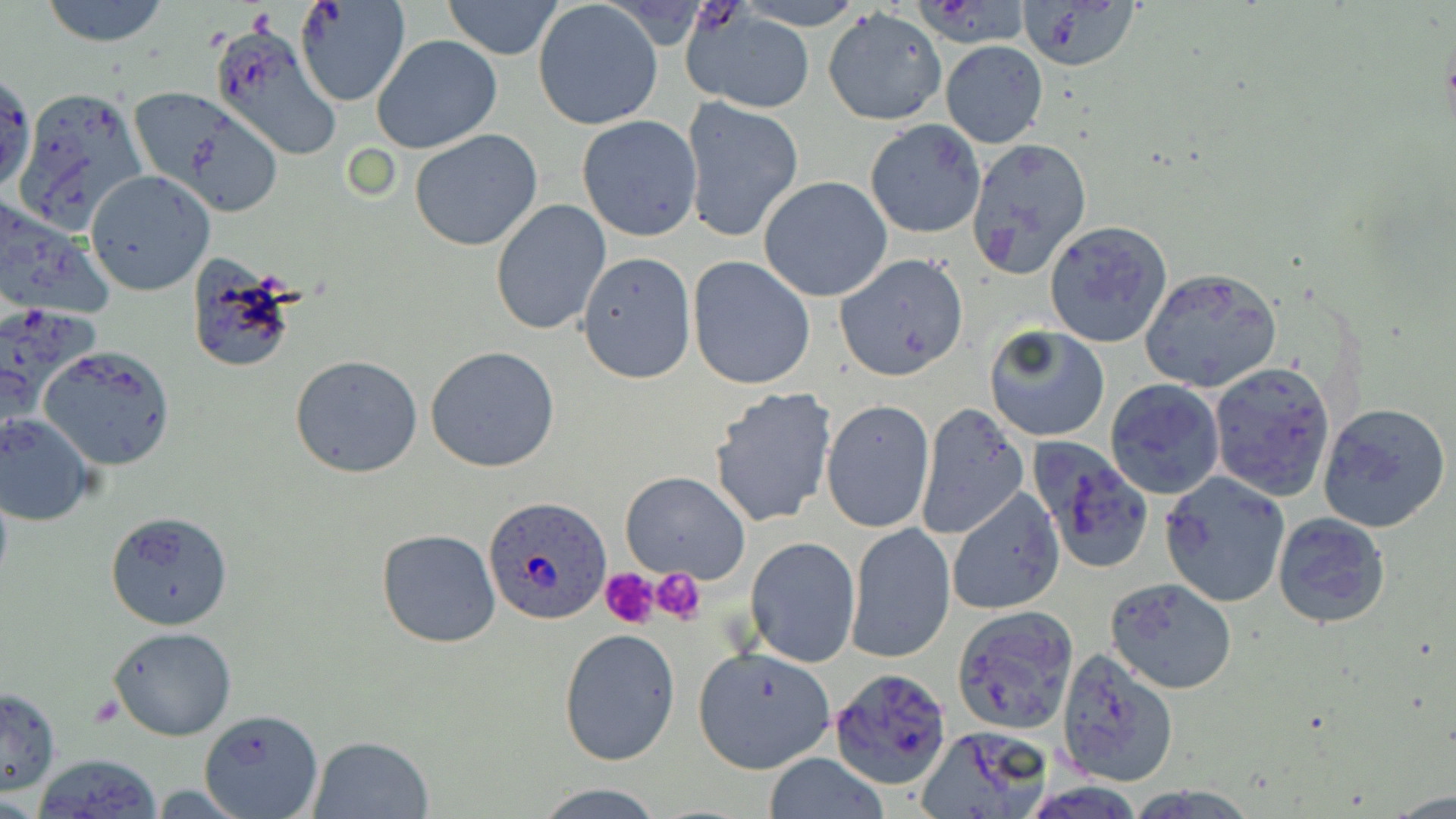

Plasmodium ovale-infected red blood cell locations = approximate bounding boxes as named x1/y1/x2/y2 corners in pixels: (x1=485, y1=496, x2=613, y2=626)
slide-level diagnosis = Plasmodium ovale
uninfected red blood cell locations = approximate bounding boxes as named x1/y1/x2/y2 corners in pixels: (x1=37, y1=0, x2=173, y2=46), (x1=297, y1=1, x2=412, y2=108), (x1=441, y1=1, x2=565, y2=60), (x1=1016, y1=1, x2=1143, y2=72), (x1=534, y1=2, x2=663, y2=130), (x1=822, y1=8, x2=946, y2=126), (x1=683, y1=9, x2=817, y2=115), (x1=209, y1=18, x2=344, y2=162), (x1=372, y1=34, x2=502, y2=155), (x1=941, y1=40, x2=1049, y2=148), (x1=1, y1=71, x2=34, y2=196), (x1=15, y1=86, x2=150, y2=232), (x1=129, y1=89, x2=277, y2=211), (x1=681, y1=97, x2=804, y2=244), (x1=577, y1=115, x2=703, y2=241), (x1=864, y1=120, x2=986, y2=238), (x1=409, y1=128, x2=543, y2=251), (x1=965, y1=138, x2=1092, y2=279), (x1=86, y1=170, x2=214, y2=296), (x1=759, y1=176, x2=893, y2=303), (x1=490, y1=200, x2=610, y2=336), (x1=1044, y1=221, x2=1173, y2=348), (x1=576, y1=252, x2=696, y2=383), (x1=833, y1=253, x2=970, y2=382), (x1=687, y1=256, x2=818, y2=390), (x1=183, y1=260, x2=302, y2=376), (x1=1139, y1=267, x2=1282, y2=393), (x1=983, y1=323, x2=1110, y2=442), (x1=40, y1=346, x2=175, y2=470), (x1=425, y1=347, x2=560, y2=472), (x1=290, y1=354, x2=423, y2=478), (x1=1208, y1=363, x2=1335, y2=501), (x1=1106, y1=378, x2=1225, y2=500), (x1=709, y1=386, x2=838, y2=528), (x1=821, y1=399, x2=935, y2=534), (x1=1319, y1=401, x2=1452, y2=533), (x1=915, y1=403, x2=1027, y2=541), (x1=1, y1=413, x2=98, y2=525), (x1=1027, y1=433, x2=1154, y2=573), (x1=1159, y1=470, x2=1290, y2=606), (x1=620, y1=471, x2=750, y2=584), (x1=949, y1=488, x2=1065, y2=615), (x1=105, y1=510, x2=233, y2=631), (x1=1271, y1=512, x2=1390, y2=630), (x1=848, y1=523, x2=954, y2=663), (x1=377, y1=528, x2=500, y2=648), (x1=746, y1=536, x2=860, y2=668), (x1=1106, y1=576, x2=1239, y2=694), (x1=951, y1=606, x2=1078, y2=733), (x1=108, y1=627, x2=236, y2=741), (x1=558, y1=628, x2=681, y2=766), (x1=693, y1=645, x2=837, y2=774), (x1=1054, y1=648, x2=1179, y2=788), (x1=826, y1=667, x2=951, y2=790), (x1=0, y1=688, x2=62, y2=795), (x1=199, y1=708, x2=324, y2=819), (x1=917, y1=727, x2=1053, y2=818), (x1=309, y1=735, x2=433, y2=819), (x1=30, y1=754, x2=161, y2=818), (x1=761, y1=754, x2=892, y2=818), (x1=531, y1=781, x2=671, y2=818)
platelet locations = approximate bounding boxes as named x1/y1/x2/y2 corners in pixels: (x1=599, y1=565, x2=663, y2=629), (x1=650, y1=567, x2=706, y2=622)
preparation = thin blood smear
stain = May-Grünwald-Giemsa
modality = optical microscopy
field of view = one of a larger specimen
image size = 1456×819 pixels
magnification = 1000x